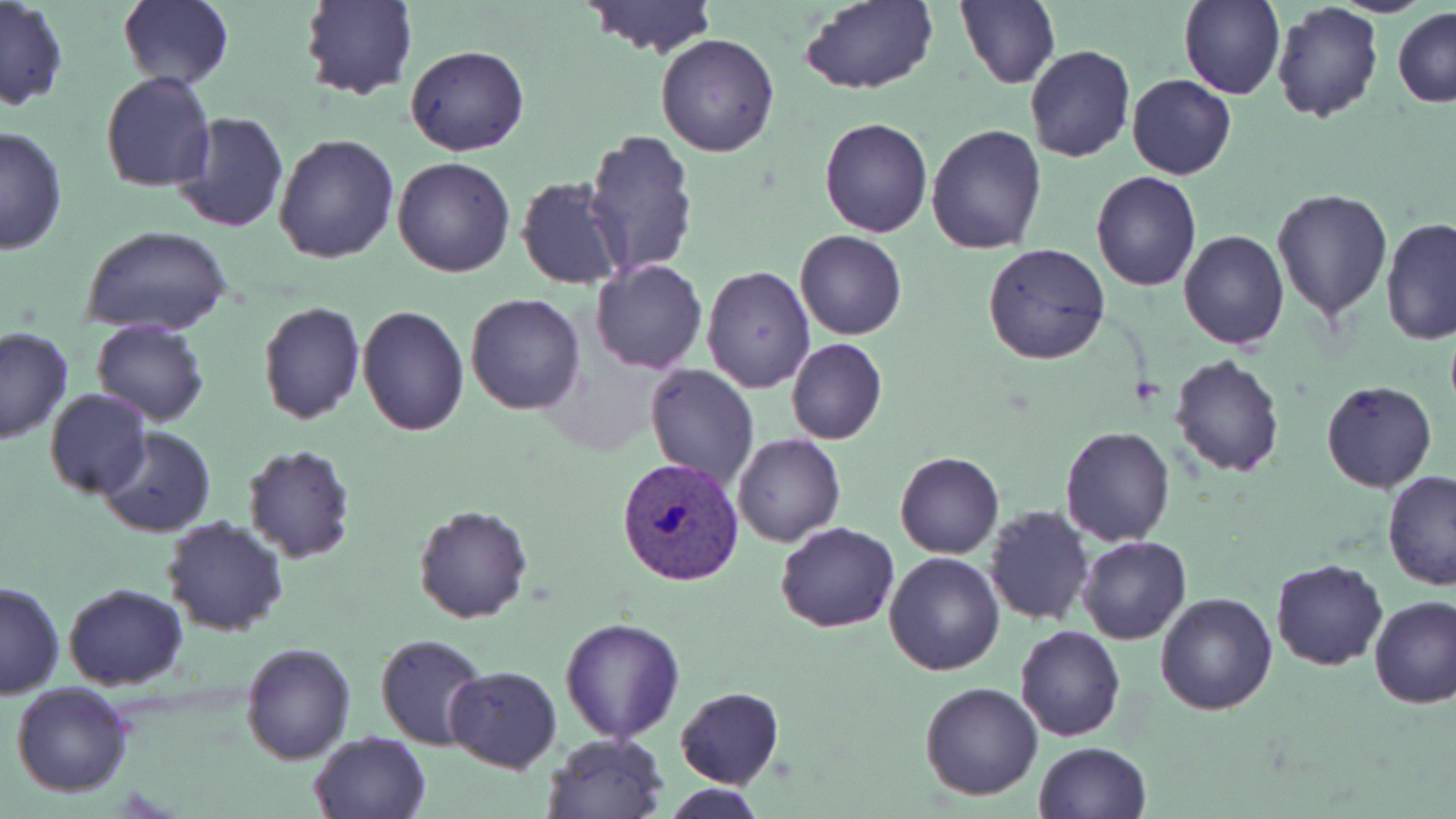

slide-level diagnosis = Plasmodium vivax
preparation = thin blood smear
field of view = one of a larger specimen
image size = 1456×819 pixels
modality = optical microscopy
stain = May-Grünwald-Giemsa
magnification = 1000x
Plasmodium vivax-infected red blood cell locations = approximate bounding boxes as (x1,y1)-(x2,y2) corner pairs in pixels: (619,457)-(745,585)
uninfected red blood cell locations = approximate bounding boxes as (x1,y1)-(x2,y2) corner pairs in pixels: (117,0)-(234,90), (300,0)-(416,101), (956,0)-(1061,90), (1180,0)-(1285,101), (582,1)-(718,58), (797,1)-(938,95), (0,2)-(69,111), (1270,2)-(1384,125), (1393,7)-(1456,108), (655,33)-(780,157), (406,44)-(529,157), (1024,45)-(1136,163), (99,72)-(217,192), (1126,74)-(1237,180), (170,110)-(290,233), (819,115)-(933,237), (0,124)-(69,254), (926,124)-(1047,252), (582,130)-(698,278), (274,133)-(400,264), (391,156)-(516,278), (1091,171)-(1201,293), (516,177)-(628,290), (1272,187)-(1395,321), (1379,217)-(1456,344), (79,224)-(232,337), (1177,229)-(1288,350), (794,230)-(908,340), (984,243)-(1110,366), (589,258)-(708,373), (701,264)-(816,394), (465,292)-(586,416), (257,300)-(366,425), (357,304)-(469,435), (90,319)-(211,427), (0,326)-(75,445), (785,338)-(887,445), (1170,354)-(1286,476), (645,363)-(759,488), (1320,379)-(1436,494), (44,390)-(150,500), (96,426)-(215,538), (1059,427)-(1176,547), (732,433)-(845,547), (240,444)-(357,564), (894,450)-(1004,559), (1383,471)-(1456,592), (412,504)-(533,624), (983,505)-(1094,625), (162,517)-(289,637), (774,522)-(901,633), (1078,534)-(1191,644), (883,551)-(1006,676), (1270,558)-(1391,672), (1,580)-(62,701), (63,583)-(188,690), (1155,591)-(1277,715), (1369,597)-(1456,709), (560,616)-(685,742), (1013,625)-(1126,742), (377,632)-(489,751), (240,643)-(356,765), (444,665)-(562,772), (919,681)-(1044,801), (11,682)-(134,798), (675,686)-(785,789), (309,731)-(432,819), (543,733)-(669,819), (1032,741)-(1152,819), (661,784)-(771,818)